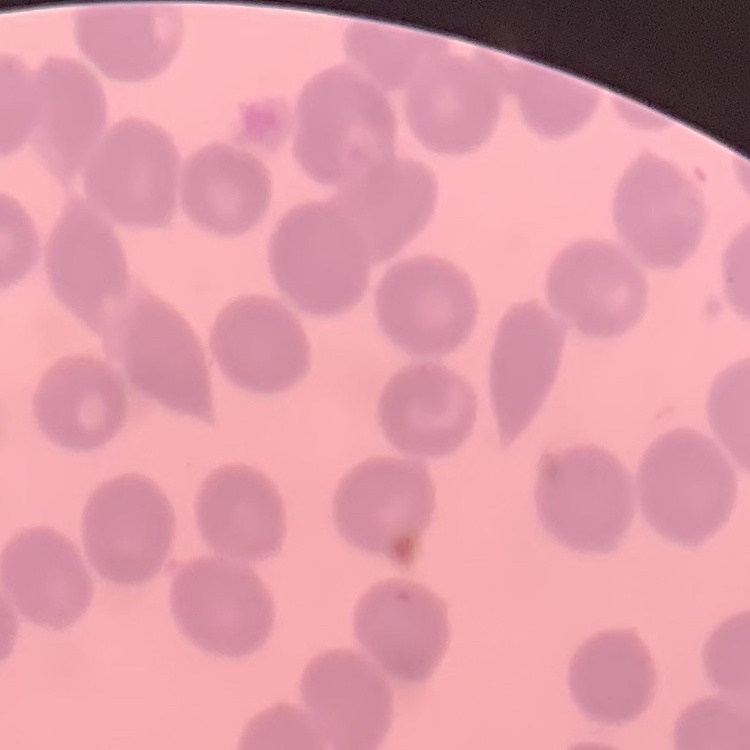
{
  "erythrocyte_morphology": "no rouleaux formation",
  "stain": "Field's or Giemsa",
  "image_type": "square crop of a larger photomicrograph",
  "preparation": "thin blood film"
}